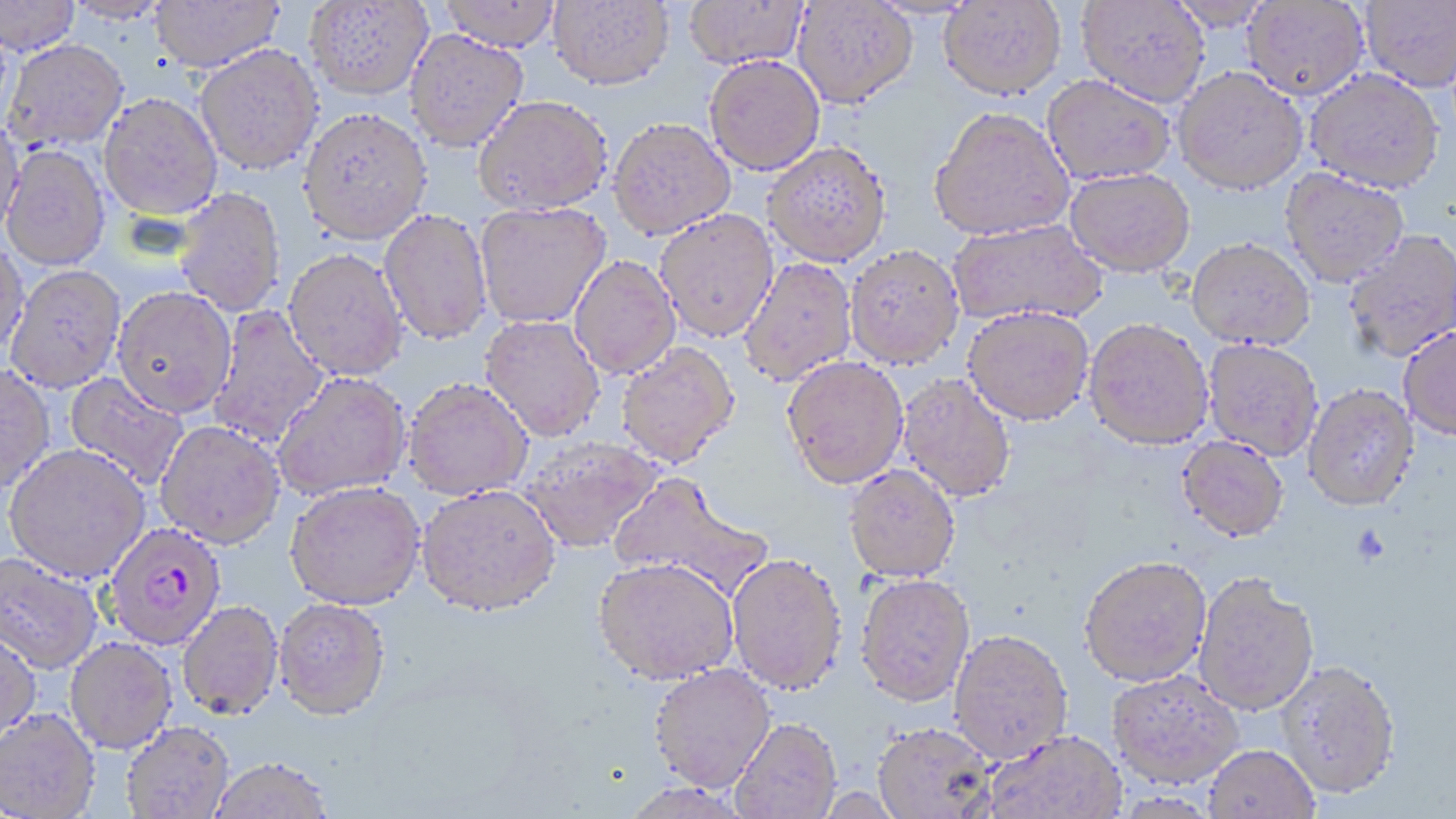

plasmodium_falciparum_infected_red_blood_cell_locations: 'approximate bounding boxes as named x1/y1/x2/y2 corners in pixels: (x1=103, y1=521, x2=227, y2=650)'
slide_level_diagnosis: Plasmodium falciparum
magnification: 1000x
uninfected_red_blood_cell_locations: 'approximate bounding boxes as named x1/y1/x2/y2 corners in pixels: (x1=0, y1=0, x2=80, y2=55), (x1=62, y1=0, x2=173, y2=25), (x1=303, y1=0, x2=433, y2=100), (x1=439, y1=0, x2=562, y2=52), (x1=548, y1=0, x2=674, y2=90), (x1=684, y1=0, x2=808, y2=69), (x1=792, y1=0, x2=918, y2=108), (x1=1077, y1=0, x2=1210, y2=106), (x1=1165, y1=0, x2=1275, y2=30), (x1=1360, y1=0, x2=1456, y2=93), (x1=149, y1=1, x2=283, y2=72), (x1=939, y1=1, x2=1066, y2=99), (x1=1242, y1=1, x2=1370, y2=100), (x1=404, y1=29, x2=529, y2=151), (x1=3, y1=38, x2=128, y2=152), (x1=195, y1=44, x2=324, y2=175), (x1=704, y1=54, x2=825, y2=175), (x1=1172, y1=65, x2=1308, y2=194), (x1=1305, y1=69, x2=1445, y2=193), (x1=1042, y1=74, x2=1175, y2=184), (x1=99, y1=92, x2=223, y2=220), (x1=473, y1=94, x2=613, y2=216), (x1=298, y1=106, x2=432, y2=245), (x1=929, y1=106, x2=1075, y2=240), (x1=0, y1=115, x2=26, y2=238), (x1=608, y1=117, x2=736, y2=239), (x1=762, y1=142, x2=891, y2=267), (x1=2, y1=144, x2=110, y2=271), (x1=1065, y1=167, x2=1195, y2=276), (x1=1279, y1=167, x2=1410, y2=287), (x1=173, y1=187, x2=286, y2=317), (x1=475, y1=202, x2=611, y2=328), (x1=379, y1=208, x2=493, y2=346), (x1=654, y1=209, x2=779, y2=342), (x1=948, y1=218, x2=1108, y2=327), (x1=1343, y1=229, x2=1456, y2=362), (x1=1186, y1=238, x2=1315, y2=350), (x1=0, y1=242, x2=29, y2=360), (x1=845, y1=245, x2=964, y2=369), (x1=283, y1=248, x2=408, y2=381), (x1=569, y1=255, x2=681, y2=379), (x1=738, y1=257, x2=858, y2=386), (x1=6, y1=264, x2=126, y2=392), (x1=112, y1=286, x2=237, y2=416), (x1=207, y1=305, x2=330, y2=450), (x1=963, y1=305, x2=1095, y2=425), (x1=479, y1=315, x2=605, y2=441), (x1=1083, y1=317, x2=1214, y2=449), (x1=1398, y1=326, x2=1456, y2=441), (x1=1203, y1=339, x2=1324, y2=459), (x1=616, y1=342, x2=740, y2=468), (x1=781, y1=355, x2=909, y2=488), (x1=0, y1=364, x2=55, y2=494), (x1=271, y1=371, x2=411, y2=500), (x1=63, y1=373, x2=189, y2=492), (x1=897, y1=373, x2=1016, y2=502), (x1=402, y1=377, x2=534, y2=500), (x1=1303, y1=383, x2=1419, y2=511), (x1=155, y1=420, x2=285, y2=548), (x1=519, y1=434, x2=664, y2=553), (x1=1176, y1=436, x2=1289, y2=542), (x1=5, y1=443, x2=150, y2=582), (x1=844, y1=464, x2=961, y2=582), (x1=608, y1=471, x2=773, y2=604), (x1=285, y1=481, x2=426, y2=610), (x1=416, y1=484, x2=561, y2=617), (x1=0, y1=552, x2=103, y2=674), (x1=727, y1=553, x2=847, y2=695), (x1=1079, y1=555, x2=1212, y2=686), (x1=593, y1=557, x2=739, y2=684), (x1=1193, y1=572, x2=1319, y2=716), (x1=856, y1=573, x2=975, y2=706), (x1=274, y1=598, x2=391, y2=720), (x1=177, y1=600, x2=284, y2=719), (x1=0, y1=625, x2=42, y2=743), (x1=948, y1=627, x2=1074, y2=763), (x1=64, y1=637, x2=177, y2=754), (x1=1275, y1=659, x2=1401, y2=800), (x1=648, y1=663, x2=777, y2=792), (x1=1108, y1=668, x2=1244, y2=788), (x1=0, y1=707, x2=101, y2=818), (x1=730, y1=717, x2=841, y2=818), (x1=121, y1=721, x2=235, y2=819), (x1=872, y1=722, x2=996, y2=818), (x1=983, y1=730, x2=1125, y2=819), (x1=1204, y1=744, x2=1319, y2=818), (x1=209, y1=757, x2=334, y2=818), (x1=617, y1=780, x2=752, y2=819)'
platelet_locations: 'approximate bounding boxes as named x1/y1/x2/y2 corners in pixels: (x1=1352, y1=526, x2=1390, y2=566)'
modality: optical microscopy
preparation: thin blood film
stain: May-Grünwald-Giemsa
field_of_view: single
image_size: 1456×819 pixels